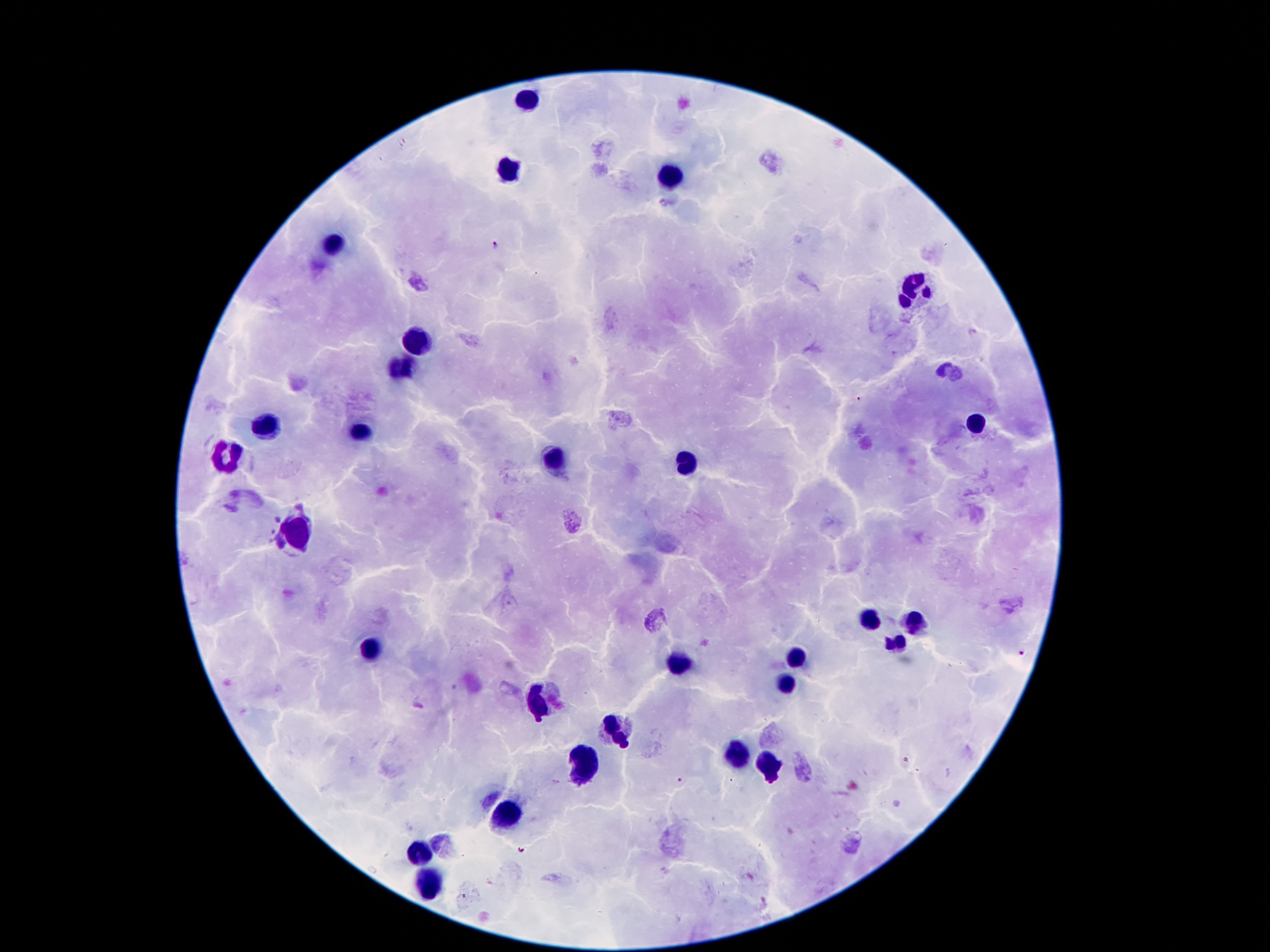

Thick peripheral-blood smear. 100x magnification. Giemsa-stained preparation. Single field of view. Image is 1270×952 pixels. Smartphone photograph taken through the microscope eyepiece. Patient malaria status: positive for Plasmodium falciparum.